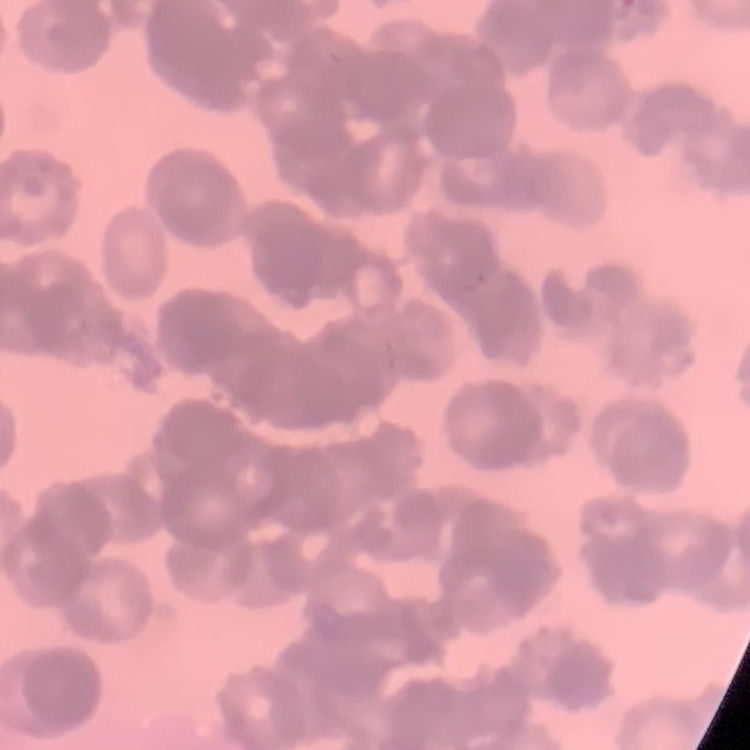 The erythrocytes exhibit rouleaux formation. Square crop of a larger photomicrograph. Field's or Giemsa stain. Thin blood smear.